Identify the parasite.
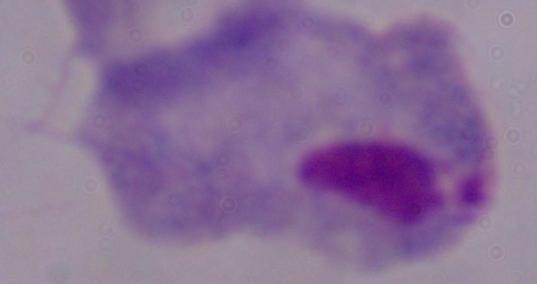
A trichomonad.

Photomicrograph. Captured at 1000x magnification.